Locate and identify every blood parasite.
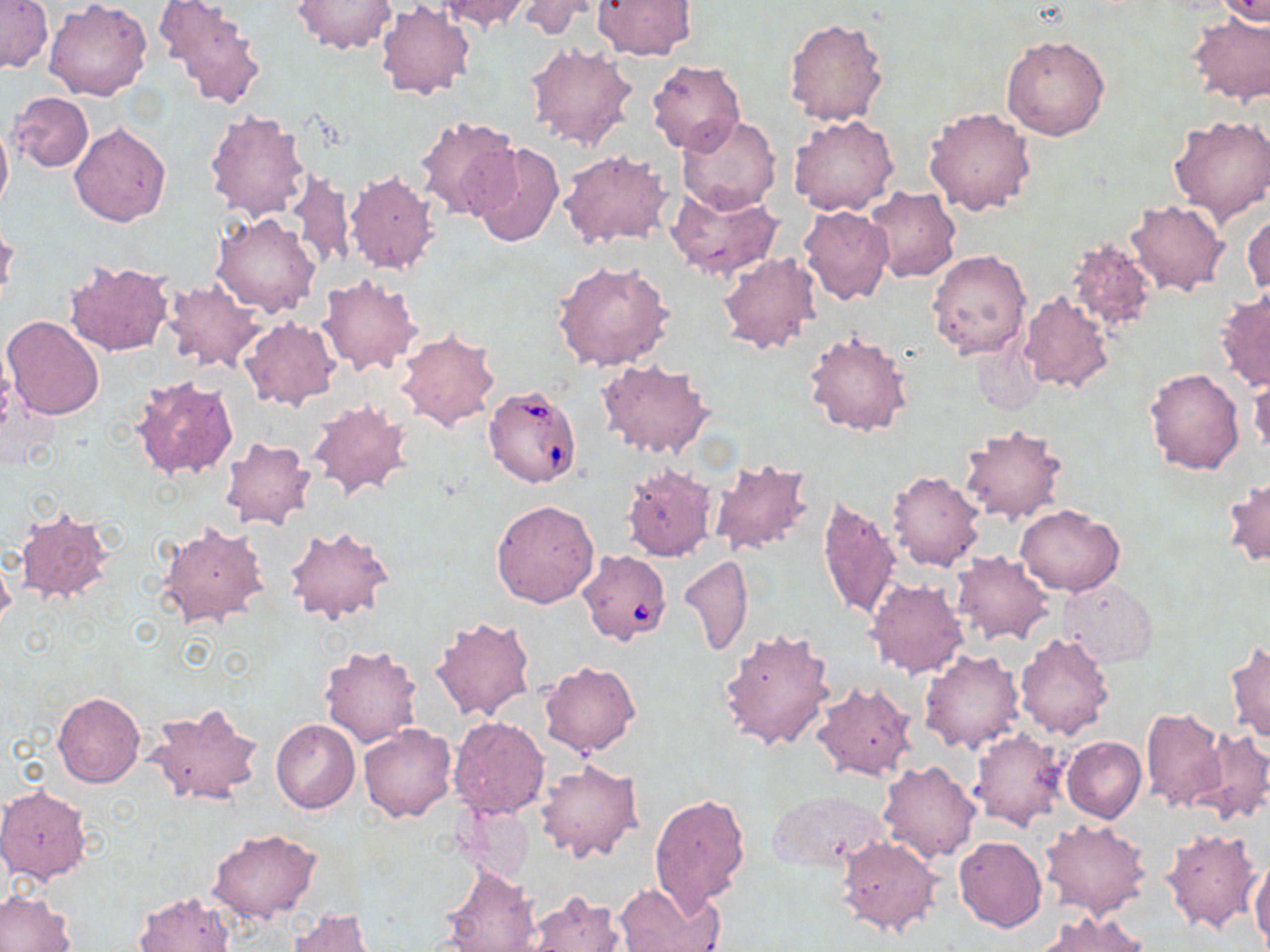
Approximate bounding boxes as [x1, y1, x2, y2] in pixels.
Babesia divergens-infected red blood cells: [483, 384, 585, 488], [575, 549, 672, 647].
No Plasmodium falciparum, Plasmodium ovale, Plasmodium malariae, Plasmodium vivax, or Trypanosoma brucei observed.

Uninfected red blood cell locations: [156, 0, 269, 110], [434, 0, 530, 33], [515, 0, 602, 39], [591, 0, 695, 59], [1217, 0, 1270, 25], [1, 1, 52, 74], [46, 1, 152, 101], [293, 1, 394, 54], [374, 2, 475, 101], [1186, 13, 1270, 106], [783, 17, 888, 127], [1001, 35, 1110, 142], [525, 40, 638, 151], [645, 59, 744, 156], [9, 92, 94, 173], [924, 107, 1035, 217], [203, 109, 312, 222], [414, 114, 522, 220], [1168, 114, 1270, 223], [788, 115, 899, 216], [676, 116, 779, 215], [0, 119, 12, 220], [70, 122, 171, 227], [471, 143, 564, 248], [558, 148, 671, 250], [343, 168, 440, 274], [289, 170, 356, 271], [666, 184, 782, 281], [866, 186, 961, 283], [1125, 200, 1229, 296], [798, 205, 893, 304], [1244, 207, 1270, 299], [211, 212, 320, 317], [0, 222, 20, 308], [1066, 235, 1158, 335], [927, 249, 1031, 359], [718, 252, 822, 355], [63, 258, 175, 357], [553, 260, 673, 370], [316, 274, 423, 376], [161, 277, 267, 373], [1215, 287, 1270, 393], [1018, 290, 1114, 393], [3, 315, 105, 421], [241, 316, 340, 408], [395, 327, 503, 431], [803, 332, 913, 437], [969, 336, 1043, 417], [596, 359, 716, 460], [1143, 366, 1246, 474], [129, 373, 240, 479], [1248, 374, 1269, 456], [305, 400, 413, 503], [957, 425, 1066, 525], [220, 436, 317, 530], [708, 457, 814, 557], [621, 463, 718, 561], [887, 468, 986, 572], [1223, 476, 1269, 568], [816, 495, 902, 623], [491, 499, 599, 607], [1015, 504, 1124, 597], [16, 506, 113, 604], [156, 520, 270, 630], [285, 526, 396, 625], [951, 550, 1055, 645], [679, 554, 753, 657], [0, 556, 16, 630], [865, 578, 968, 680], [1059, 578, 1157, 667], [698, 579, 804, 712], [432, 617, 536, 722], [718, 627, 834, 751], [1014, 633, 1116, 740], [1226, 640, 1270, 744], [320, 645, 423, 747], [918, 650, 1026, 754], [540, 659, 642, 757], [811, 682, 919, 783], [53, 692, 145, 788], [145, 704, 263, 808], [1140, 707, 1228, 814], [448, 716, 551, 819], [271, 719, 360, 812], [360, 723, 457, 822], [969, 727, 1068, 831], [1192, 730, 1270, 824], [1061, 736, 1146, 824], [536, 759, 643, 863], [878, 760, 981, 863], [0, 785, 92, 884], [767, 787, 891, 871], [649, 793, 752, 910], [457, 801, 533, 886], [1039, 818, 1151, 920], [1162, 826, 1264, 934], [208, 830, 321, 923], [834, 835, 943, 937], [954, 836, 1047, 932], [1250, 859, 1270, 949], [440, 867, 540, 952], [612, 882, 723, 952], [0, 891, 75, 952], [522, 891, 628, 952], [135, 892, 235, 952], [288, 908, 375, 952], [1039, 911, 1149, 952]. Slide-level diagnosis: Babesia divergens. Light microscopy. May-Grünwald-Giemsa stain. Thin blood smear. Image is 1270×952 pixels. One field of a larger specimen. 1000x magnification.